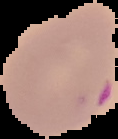
{
  "malaria_status": "parasitized",
  "preparation": "thin blood smear",
  "image_type": "cell region segmented out of the field of view; surrounding area masked to black",
  "image_size": "118×139 pixels"
}